Give the extent of all uninfected red blood cells.
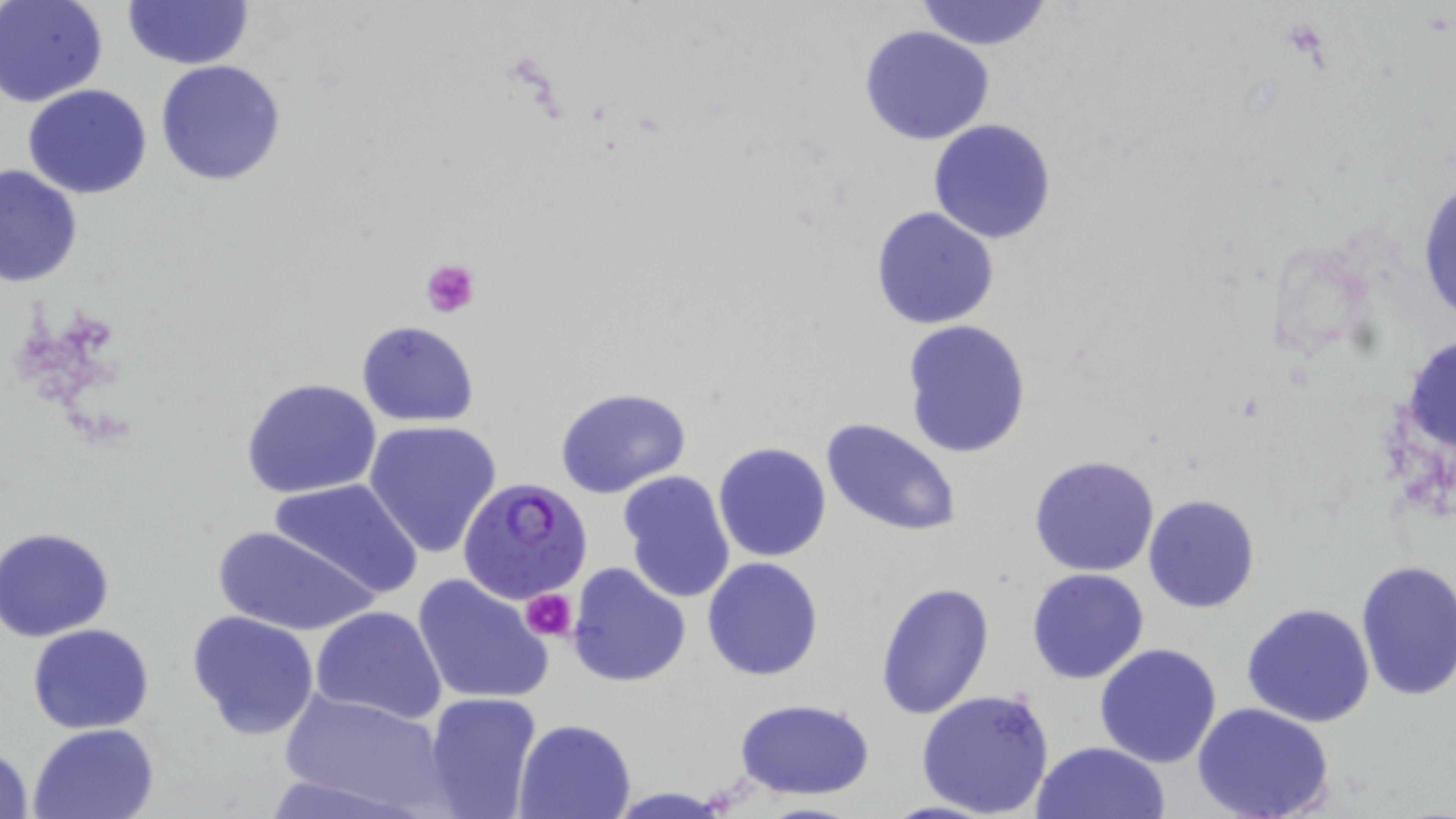

Approximate bounding boxes as named x1/y1/x2/y2 corners in pixels.
Uninfected red blood cells: (x1=2, y1=0, x2=108, y2=106), (x1=914, y1=0, x2=1054, y2=49), (x1=123, y1=1, x2=254, y2=71), (x1=859, y1=25, x2=994, y2=145), (x1=156, y1=59, x2=288, y2=186), (x1=23, y1=84, x2=151, y2=199), (x1=927, y1=120, x2=1057, y2=244), (x1=0, y1=163, x2=83, y2=286), (x1=1416, y1=171, x2=1455, y2=334), (x1=870, y1=206, x2=999, y2=331), (x1=902, y1=320, x2=1032, y2=459), (x1=356, y1=321, x2=479, y2=426), (x1=241, y1=378, x2=383, y2=500), (x1=554, y1=386, x2=691, y2=499), (x1=820, y1=417, x2=963, y2=538), (x1=364, y1=420, x2=503, y2=559), (x1=713, y1=442, x2=832, y2=564), (x1=1027, y1=454, x2=1161, y2=577), (x1=616, y1=470, x2=737, y2=604), (x1=270, y1=477, x2=425, y2=601), (x1=1141, y1=493, x2=1260, y2=615), (x1=213, y1=525, x2=379, y2=637), (x1=1, y1=528, x2=118, y2=641), (x1=701, y1=557, x2=824, y2=682), (x1=1354, y1=559, x2=1456, y2=701), (x1=567, y1=561, x2=692, y2=687), (x1=1026, y1=568, x2=1148, y2=684), (x1=412, y1=572, x2=554, y2=708), (x1=876, y1=582, x2=996, y2=720), (x1=1241, y1=603, x2=1376, y2=728), (x1=310, y1=605, x2=447, y2=725), (x1=186, y1=609, x2=320, y2=740), (x1=27, y1=623, x2=155, y2=733), (x1=1094, y1=643, x2=1223, y2=769), (x1=278, y1=688, x2=452, y2=816), (x1=915, y1=688, x2=1056, y2=818), (x1=424, y1=691, x2=543, y2=819), (x1=734, y1=698, x2=877, y2=801), (x1=1191, y1=701, x2=1336, y2=819), (x1=514, y1=717, x2=637, y2=818), (x1=28, y1=722, x2=159, y2=818), (x1=1030, y1=740, x2=1168, y2=819), (x1=0, y1=743, x2=33, y2=819), (x1=257, y1=774, x2=416, y2=818), (x1=605, y1=788, x2=735, y2=817), (x1=747, y1=801, x2=869, y2=819).

Summary:
  - Platelet locations: (x1=1282, y1=15, x2=1330, y2=62), (x1=421, y1=259, x2=479, y2=317), (x1=521, y1=587, x2=575, y2=643)
  - Plasmodium falciparum-infected red blood cell locations: (x1=458, y1=475, x2=593, y2=606)
  - Slide-level diagnosis: Plasmodium falciparum
  - Preparation: thin blood film
  - Image size: 1456×819 pixels
  - Stain: May-Grünwald-Giemsa
  - Field of view: one of a larger specimen
  - Modality: optical microscopy
  - Magnification: 1000x